Describe the morphology of the erythrocytes.
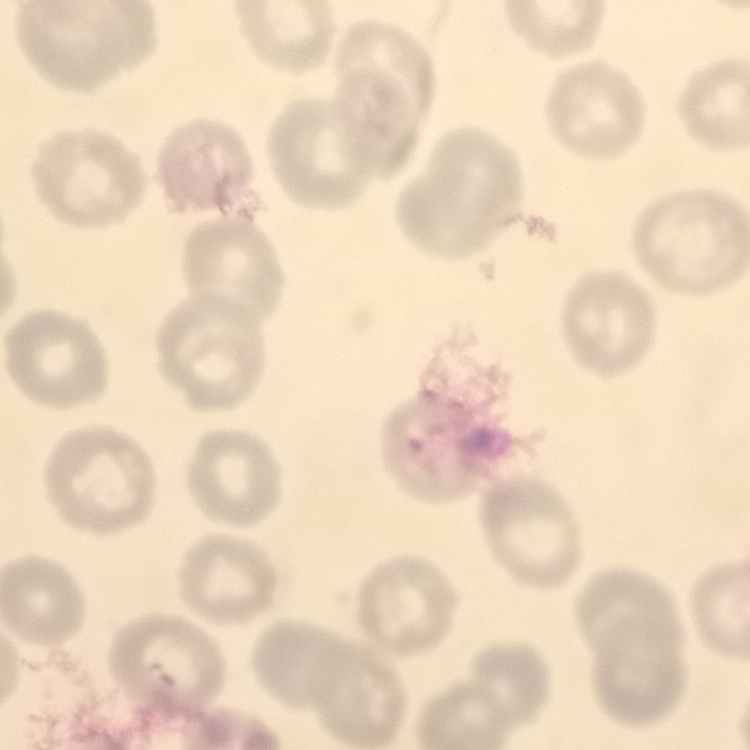

No rouleaux formation.

Summary:
  - Stain: Field's or Giemsa
  - Preparation: thin peripheral smear
  - Image type: square crop of a larger photomicrograph